Evaluate for malaria.
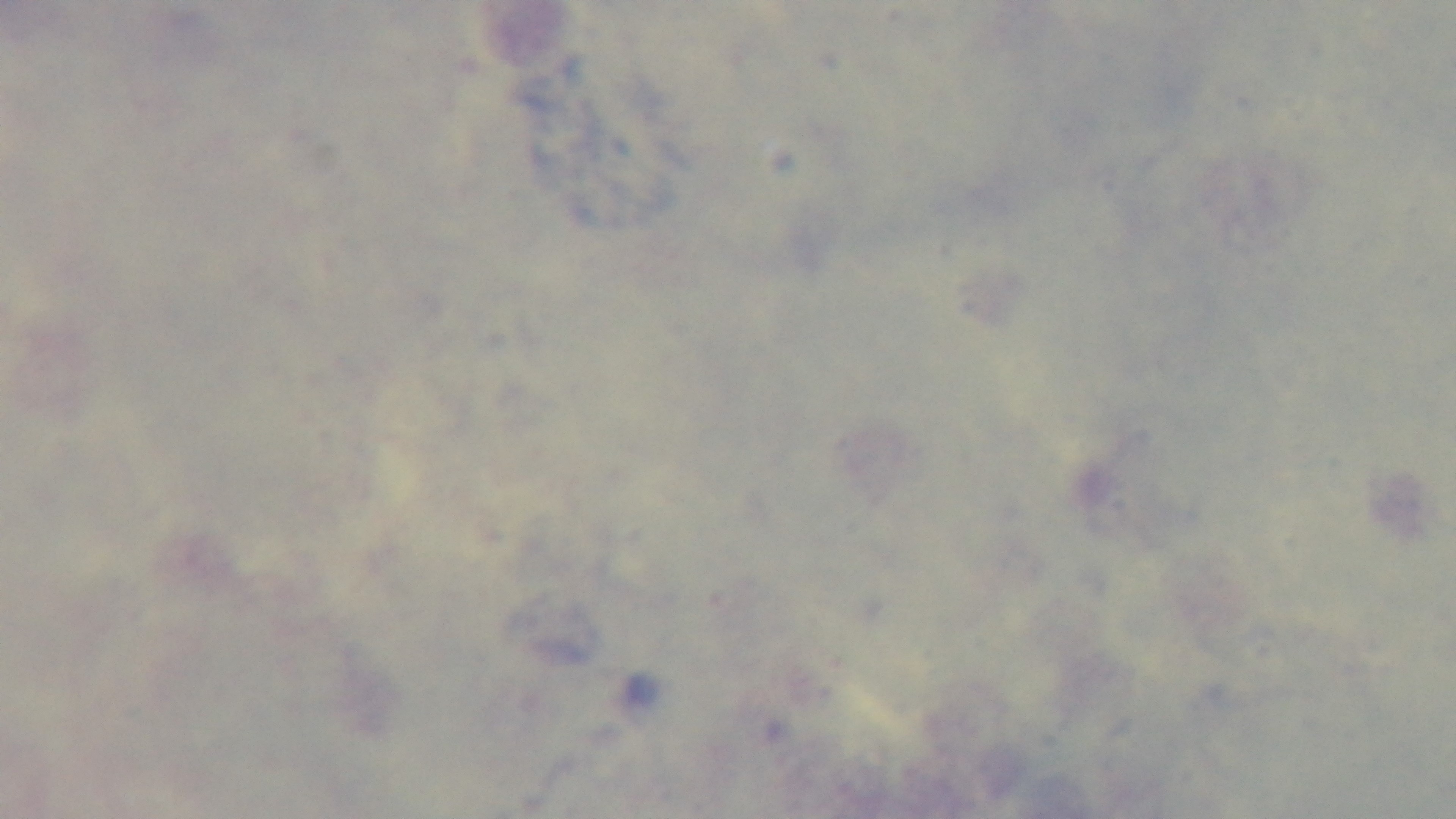

It is uninfected.

stain: Giemsa
modality: light microscopy
objective: 100x oil immersion
preparation: thick blood film
capture: mounted 4K digital camera
field_of_view: single